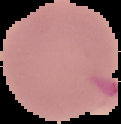 Cell region segmented out of the field of view; the surrounding area is masked to black. Image is 121×124 pixels. From a thin blood film. Malaria status: uninfected.